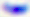

magnification = 400x
modality = micrograph
identification = Toxoplasma gondii